Assess this cell for malaria.
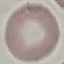

Uninfected.

Summary:
  - Preparation: thin blood smear
  - Capture: smartphone camera at the microscope eyepiece
  - Stain: Giemsa
  - Image type: cell patch, automatically extracted from a larger field of view and resized to 64 × 64 pixels